Locate every Plasmodium parasite.
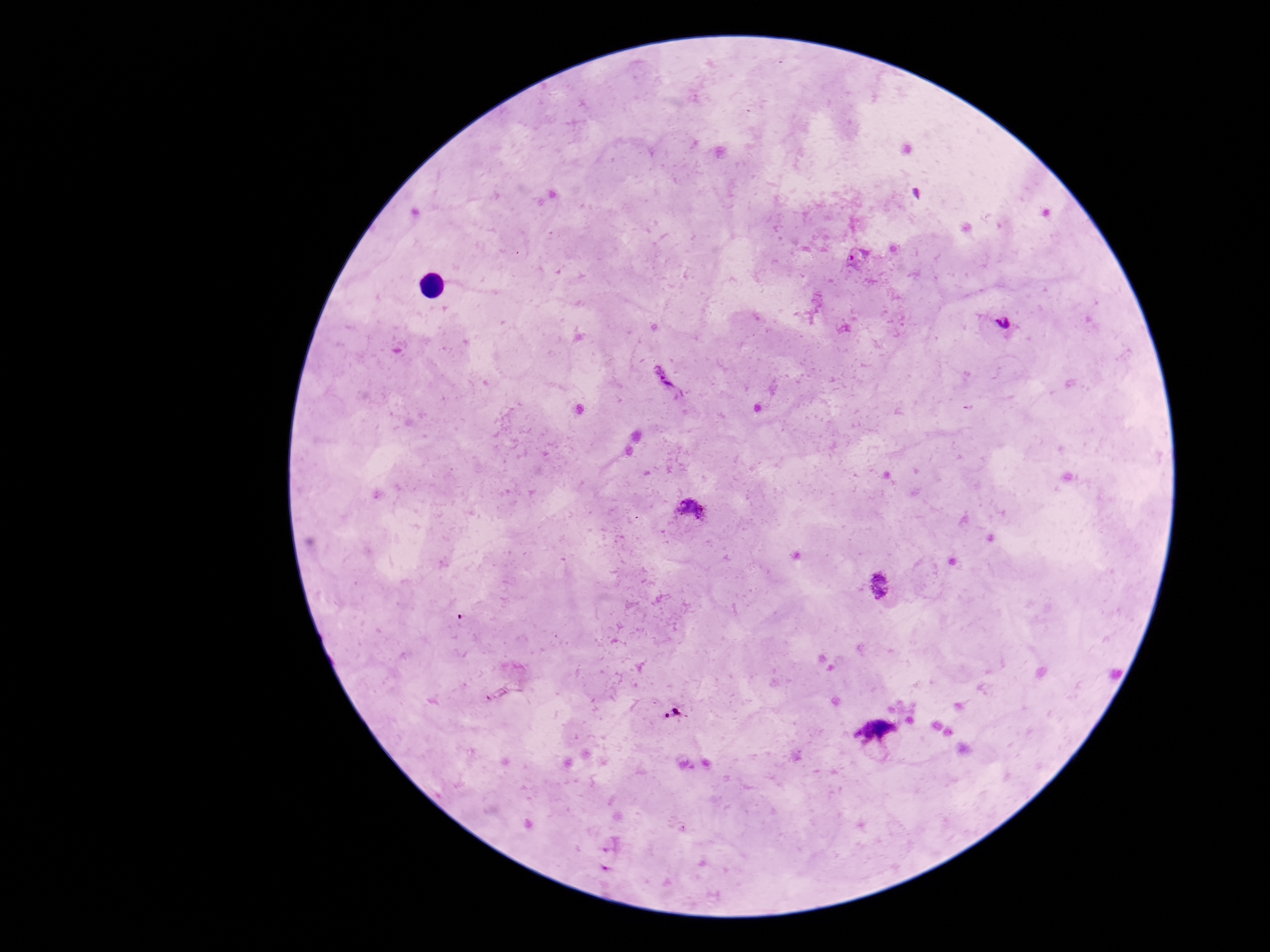
Approximate centers as (x, y) in pixels.
Plasmodium parasites: (861, 258), (1005, 326), (668, 382), (691, 507), (880, 584), (675, 713), (877, 729).

patient_malaria_status: infected
field_of_view: single
preparation: thick blood smear
capture: smartphone camera through the microscope eyepiece
magnification: 100x
image_size: 1270×952 pixels
stain: Giemsa